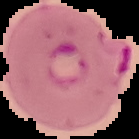
Summary:
  - Image size: 139×139 pixels
  - Result: Plasmodium parasites detected
  - Image type: segmented cell region on a black background
  - Preparation: thin blood film